Comment on the morphology of the erythrocytes.
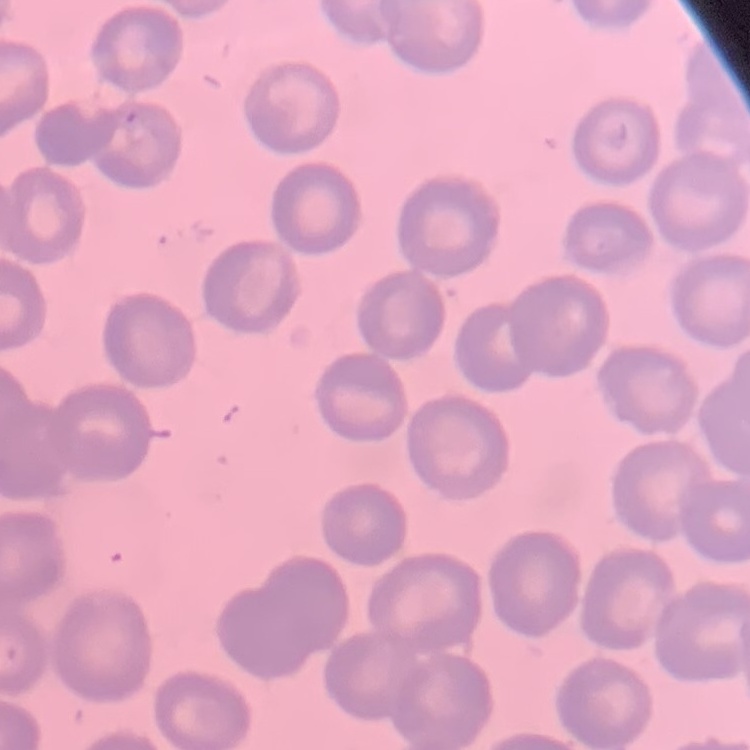

No rouleaux formation.

Stained with either Field's or Giemsa. Thin blood smear. One tile cut from a larger photomicrograph.